State which parasite is depicted.
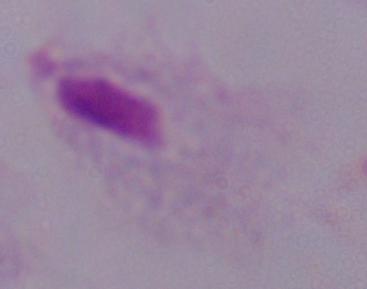
A trichomonad.

{
  "magnification": "1000x",
  "modality": "photomicrograph"
}